Assess this cell for malaria.
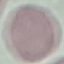

Uninfected.

Summary:
  - Stain: Giemsa
  - Preparation: thin blood smear
  - Capture: smartphone through the microscope eyepiece
  - Image type: cell patch, automatically extracted from a larger field of view and resized to 64 × 64 pixels